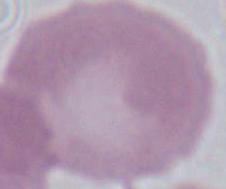
{
  "modality": "photomicrograph",
  "magnification": "1000x",
  "identification": "erythrocyte"
}